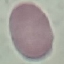
result: no malaria parasites seen
preparation: thin blood film
capture: smartphone through the microscope eyepiece
stain: Giemsa
image_type: automatically extracted cell patch, resized to 64 × 64 pixels